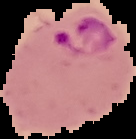

image_type: segmented cell region with the area outside set to black
image_size: 136×139 pixels
preparation: thin blood film
result: malaria parasites identified